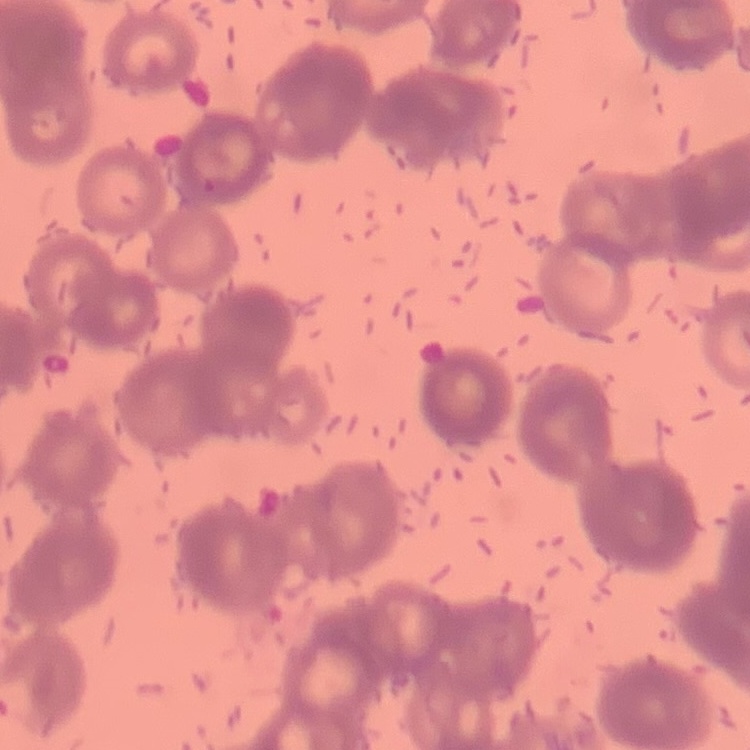

erythrocyte morphology = rouleaux formation
preparation = thin blood film
image type = one tile cut from a larger photomicrograph
stain = Field's or Giemsa